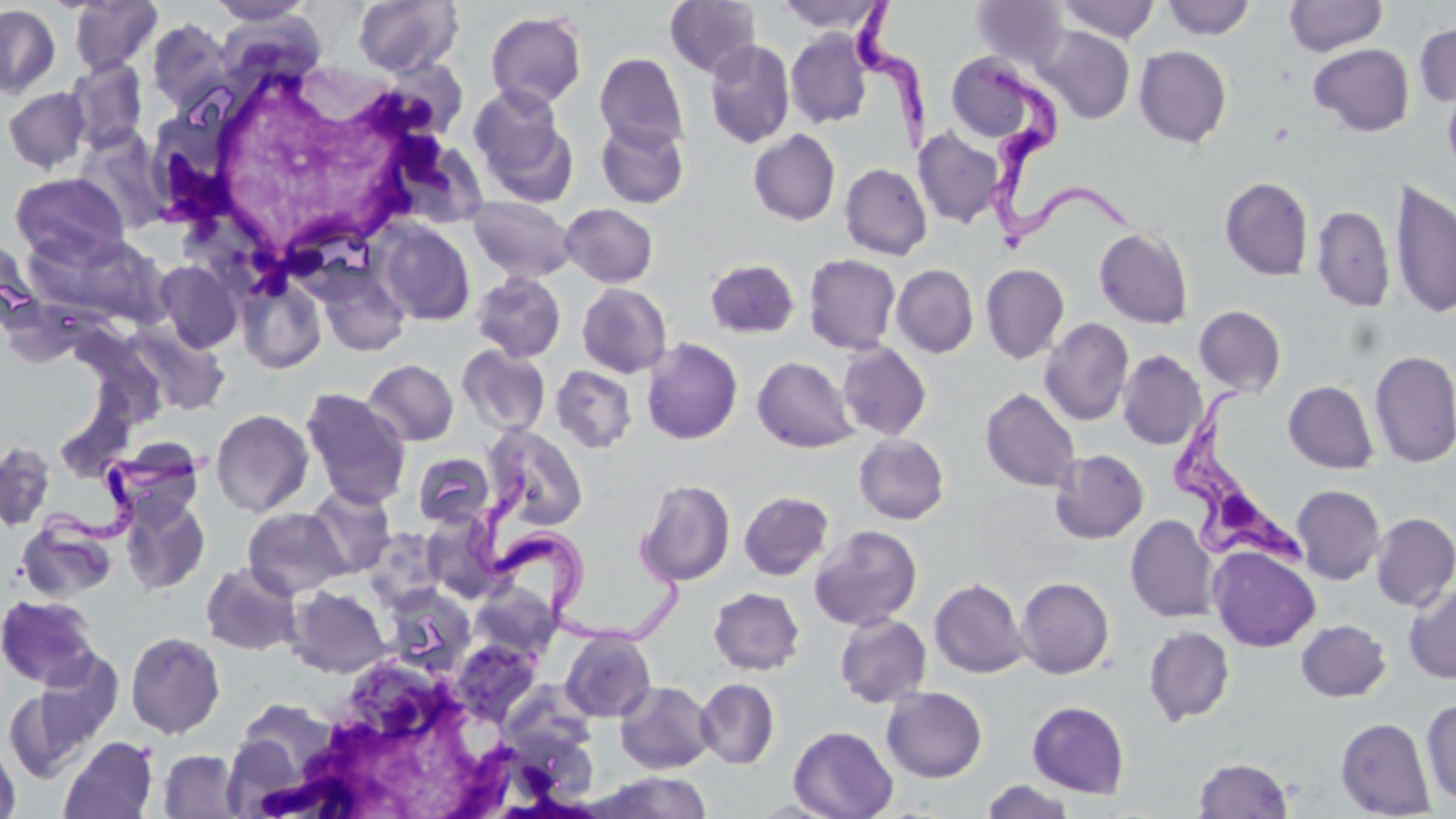
Summary:
  - Coordinate format: approximate bounding boxes as (x1,y1)-(x2,y2) corner pairs in pixels
  - Trypanosoma brucei locations: (853,0)-(934,155), (976,63)-(1136,247), (1169,379)-(1310,578), (40,443)-(220,592), (469,474)-(688,650)
  - Uninfected red blood cell locations: (68,0)-(163,75), (352,0)-(463,76), (665,0)-(762,78), (1056,0)-(1160,43), (1162,0)-(1256,40), (1284,0)-(1388,56), (207,1)-(316,26), (774,1)-(888,34), (971,1)-(1070,69), (0,4)-(61,99), (485,11)-(587,110), (146,19)-(234,111), (1414,23)-(1456,107), (1036,26)-(1135,124), (785,29)-(873,129), (704,40)-(795,149), (1308,43)-(1415,137), (1134,46)-(1232,147), (595,52)-(689,152), (946,53)-(1045,146), (65,59)-(148,151), (1441,75)-(1456,179), (468,85)-(576,203), (2,87)-(91,173), (595,119)-(690,209), (914,128)-(1005,228), (748,129)-(841,226), (73,131)-(173,235), (840,163)-(932,260), (9,172)-(129,267), (1219,176)-(1314,281), (1389,179)-(1456,320), (467,196)-(577,283), (560,203)-(659,287), (1312,205)-(1395,312), (376,220)-(476,326), (1094,227)-(1193,329), (43,233)-(174,326), (803,254)-(901,354), (704,259)-(800,339), (152,260)-(243,353), (314,262)-(411,357), (981,263)-(1070,364), (891,264)-(979,358), (470,272)-(567,363), (237,276)-(327,374), (577,283)-(672,378), (1194,305)-(1286,397), (1040,317)-(1134,426), (122,322)-(231,420), (641,337)-(743,444), (837,342)-(931,441), (457,346)-(550,436), (1117,350)-(1207,450), (1369,350)-(1456,469), (752,356)-(858,453), (363,359)-(459,446), (550,365)-(637,453), (1283,380)-(1379,474), (300,387)-(412,509), (980,388)-(1081,492), (211,409)-(313,517), (482,424)-(588,530), (854,433)-(950,524), (103,439)-(205,525), (0,442)-(56,532), (1050,449)-(1149,543), (413,452)-(495,528), (636,479)-(736,587), (305,484)-(397,578), (1291,484)-(1386,584), (739,491)-(833,580), (119,494)-(210,596), (243,507)-(348,598), (1371,512)-(1456,611), (422,513)-(504,602), (1125,515)-(1219,623), (17,519)-(116,603), (809,524)-(923,631), (362,527)-(445,611), (1209,546)-(1321,652), (201,562)-(302,656), (1015,577)-(1115,679), (929,578)-(1030,679), (469,582)-(559,661), (1403,582)-(1456,684), (381,584)-(477,676), (287,585)-(391,677), (709,587)-(805,676), (1,595)-(100,688), (834,613)-(932,708), (1296,619)-(1391,702), (1143,625)-(1235,726), (560,628)-(656,722), (126,632)-(226,739), (452,640)-(542,725), (695,678)-(780,769), (615,680)-(716,774), (3,684)-(103,782), (881,687)-(987,782), (226,698)-(349,807), (1422,699)-(1456,807), (1027,701)-(1130,798), (1335,717)-(1436,818), (788,726)-(898,819), (59,736)-(158,819), (0,738)-(21,819), (158,749)-(242,818), (1193,757)-(1293,817), (597,771)-(713,819), (981,779)-(1076,819)
  - White blood cell locations: (170,52)-(456,289), (244,651)-(564,818)
  - Slide-level diagnosis: Trypanosoma brucei
  - Magnification: 1000x
  - Stain: May-Grünwald-Giemsa
  - Image size: 1456×819 pixels
  - Field of view: single
  - Modality: optical microscopy
  - Preparation: thin blood smear